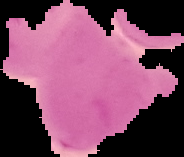 Cell region segmented out of the field of view; the surrounding area is masked to black. From a thin blood film. Malaria status: uninfected. Image is 184×157 pixels.